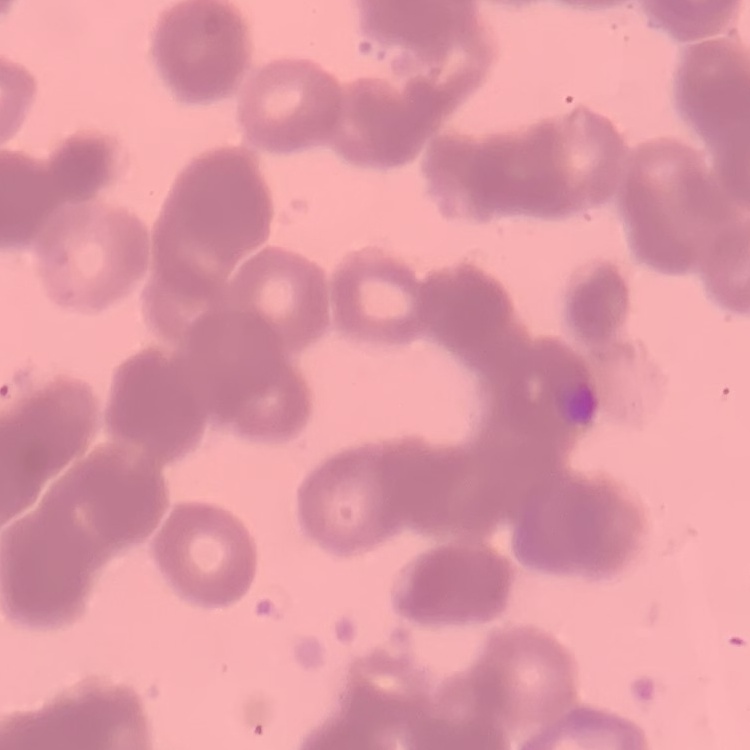 The erythrocytes show rouleaux formation. Field's or Giemsa stain. Thin blood film. One tile cut from a larger photomicrograph.